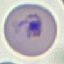
Summary:
  - Malaria status: parasitized
  - Stain: Giemsa
  - Image type: cell patch, automatically extracted from a larger field of view and resized to 64 × 64 pixels
  - Capture: smartphone camera at the microscope eyepiece
  - Preparation: thin smear